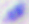
Captured at 400x magnification. Toxoplasma gondii is seen. Photomicrograph.